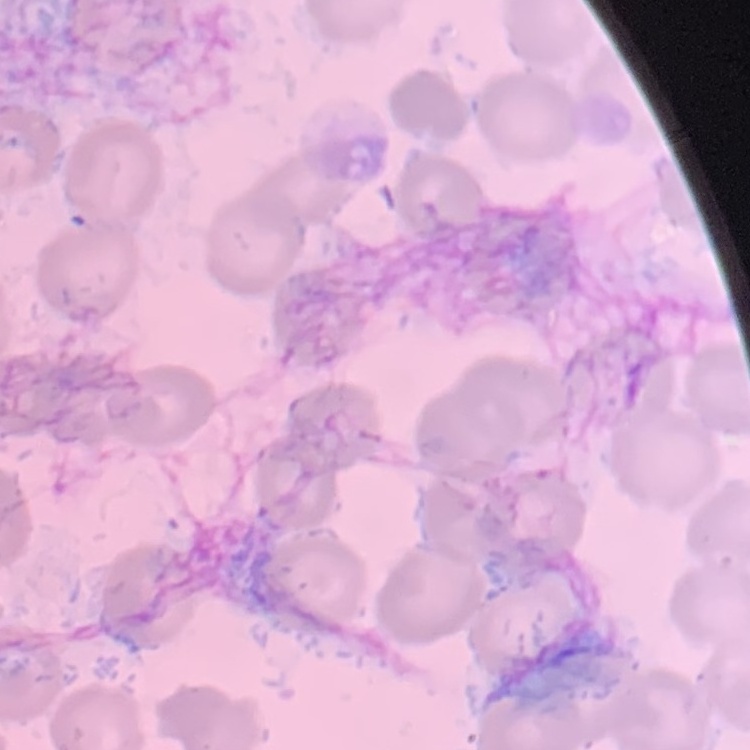
Summary:
  - Erythrocyte morphology: no rouleaux formation
  - Stain: Field's or Giemsa
  - Image type: square crop of a larger photomicrograph
  - Preparation: thin blood smear